Outline each blood parasite and name the species.
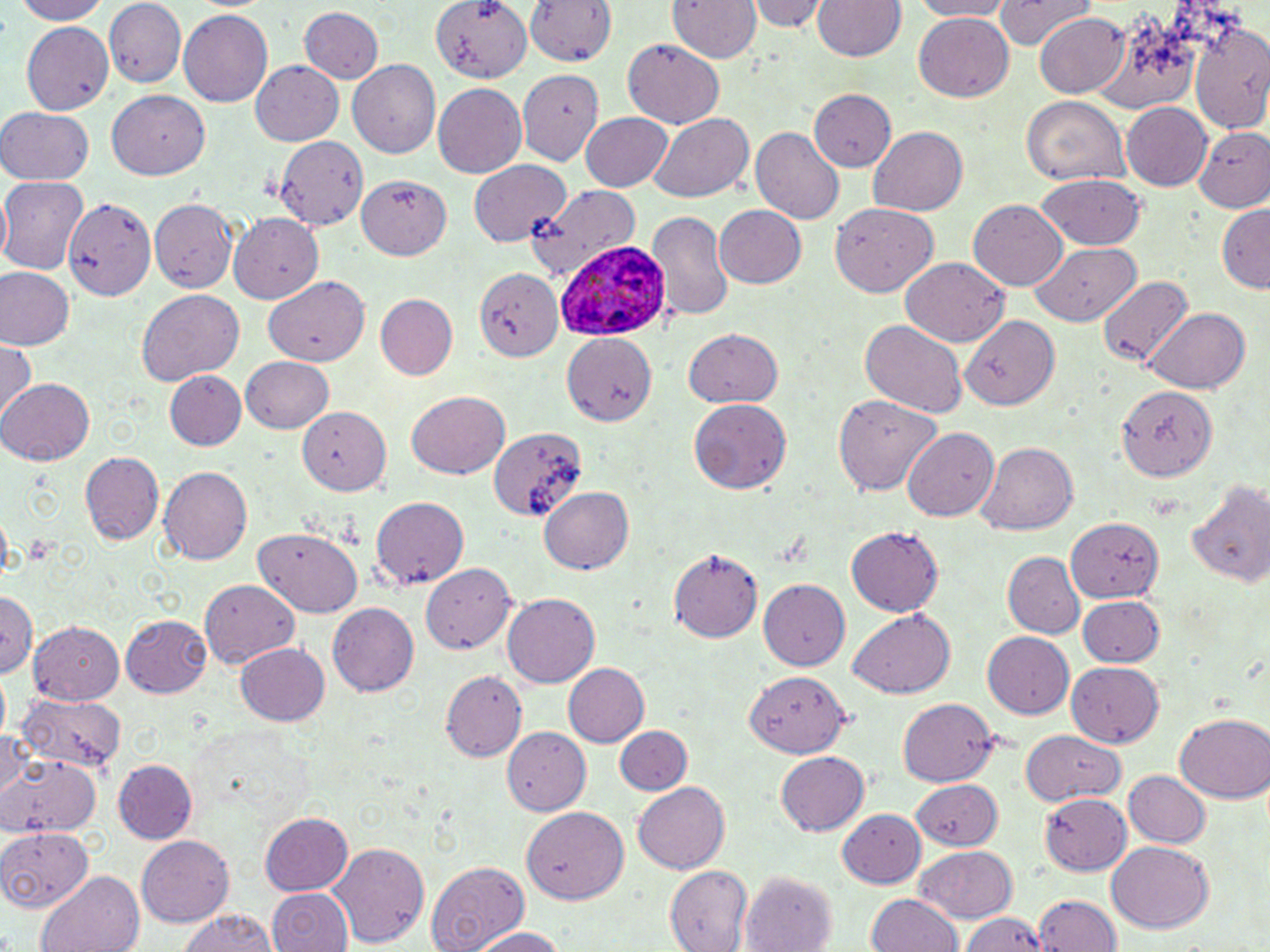
Approximate bounding boxes as [x1, y1, x2, y2] in pixels.
Plasmodium ovale-infected red blood cells: [560, 234, 687, 341].
No Plasmodium falciparum, Plasmodium malariae, Plasmodium vivax, Babesia divergens, or Trypanosoma brucei observed.

Summary:
  - White blood cell locations: [525, 1, 618, 68]
  - Uninfected red blood cell locations: [7, 0, 112, 24], [427, 0, 530, 82], [748, 0, 827, 32], [811, 0, 907, 62], [907, 0, 1017, 20], [994, 0, 1096, 50], [669, 1, 760, 64], [105, 3, 186, 85], [297, 6, 383, 84], [180, 9, 273, 109], [1033, 11, 1130, 99], [913, 13, 1014, 104], [21, 19, 116, 116], [1190, 19, 1270, 134], [622, 40, 723, 128], [249, 61, 343, 147], [347, 61, 440, 158], [518, 68, 604, 165], [433, 83, 528, 178], [108, 89, 212, 181], [808, 90, 894, 172], [1021, 95, 1130, 185], [1121, 102, 1213, 190], [0, 107, 95, 183], [580, 110, 675, 190], [648, 113, 754, 204], [1192, 125, 1270, 212], [751, 127, 843, 225], [867, 128, 968, 216], [274, 134, 372, 229], [468, 160, 570, 245], [1038, 173, 1145, 249], [357, 174, 451, 259], [2, 175, 90, 274], [528, 186, 646, 279], [152, 198, 238, 291], [968, 199, 1070, 291], [64, 200, 157, 303], [1216, 202, 1270, 292], [712, 203, 807, 289], [829, 203, 936, 295], [647, 209, 734, 325], [230, 212, 323, 302], [1030, 242, 1143, 326], [900, 258, 1011, 346], [471, 262, 564, 366], [0, 268, 75, 350], [267, 275, 369, 366], [1098, 275, 1194, 369], [135, 289, 244, 386], [377, 296, 457, 380], [1148, 306, 1250, 391], [961, 313, 1058, 409], [859, 319, 966, 416], [682, 328, 784, 408], [563, 335, 656, 425], [0, 340, 37, 423], [239, 356, 334, 432], [166, 371, 246, 451], [0, 377, 93, 466], [1117, 387, 1216, 480], [833, 389, 940, 494], [407, 391, 509, 480], [690, 400, 791, 497], [300, 407, 390, 497], [485, 424, 585, 525], [901, 427, 999, 523], [980, 441, 1076, 536], [80, 450, 163, 546], [160, 466, 253, 564], [1185, 478, 1270, 591], [540, 486, 637, 575], [370, 495, 469, 589], [1068, 515, 1163, 602], [845, 524, 946, 616], [256, 525, 363, 614], [670, 546, 761, 642], [1001, 552, 1083, 640], [420, 564, 516, 654], [201, 578, 299, 668], [758, 580, 851, 670], [1, 590, 38, 682], [503, 594, 598, 687], [1076, 597, 1166, 665], [327, 600, 419, 693], [848, 610, 955, 698], [123, 615, 210, 697], [28, 620, 126, 704], [981, 632, 1074, 720], [234, 642, 329, 726], [564, 662, 651, 747], [1067, 662, 1165, 750], [744, 669, 851, 757], [440, 671, 525, 761], [20, 691, 124, 775], [898, 699, 997, 789], [1174, 713, 1270, 803], [0, 723, 30, 800], [614, 725, 693, 795], [502, 728, 590, 813], [1021, 729, 1125, 809], [774, 749, 869, 835], [0, 753, 103, 838], [114, 760, 196, 843], [1123, 769, 1210, 847], [912, 778, 1003, 849], [632, 783, 728, 874], [1039, 795, 1132, 875], [838, 807, 925, 888], [522, 808, 629, 906], [261, 813, 354, 893], [0, 827, 91, 913], [136, 835, 233, 926], [329, 841, 431, 949], [1106, 842, 1216, 935], [916, 846, 1019, 924], [425, 859, 530, 952], [663, 865, 750, 950], [739, 869, 838, 952], [34, 870, 144, 952], [266, 888, 352, 952], [866, 894, 964, 952], [1034, 894, 1118, 952], [175, 908, 281, 952], [960, 911, 1047, 952], [467, 926, 570, 951]
  - Slide-level diagnosis: Plasmodium ovale
  - Field of view: one of a larger specimen
  - Modality: light microscopy
  - Stain: May-Grünwald-Giemsa
  - Magnification: 1000x
  - Preparation: thin blood film
  - Image size: 1270×952 pixels